Assess the morphology of the erythrocytes.
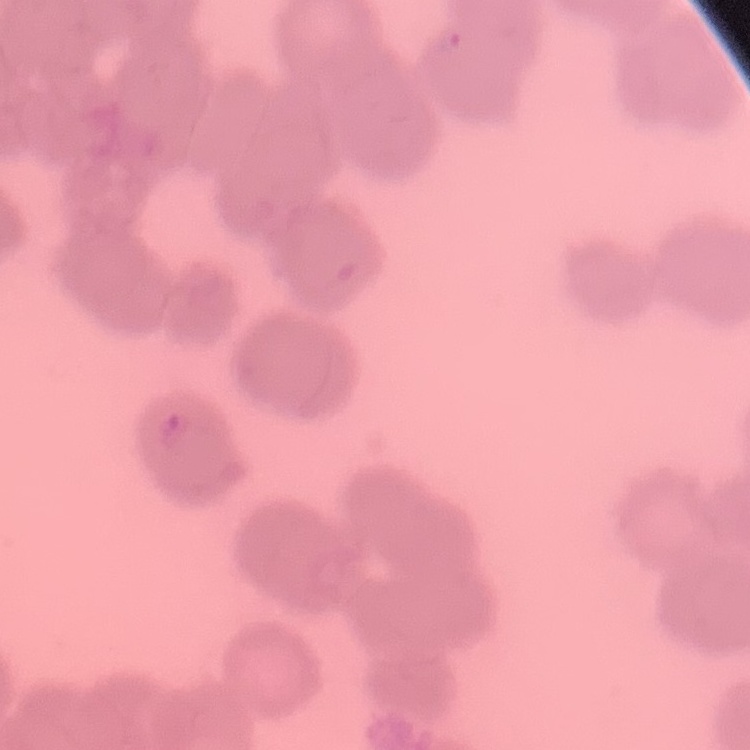
They show rouleaux formation.

Summary:
  - Image type: one tile cut from a larger photomicrograph
  - Stain: Field's or Giemsa
  - Preparation: thin blood smear